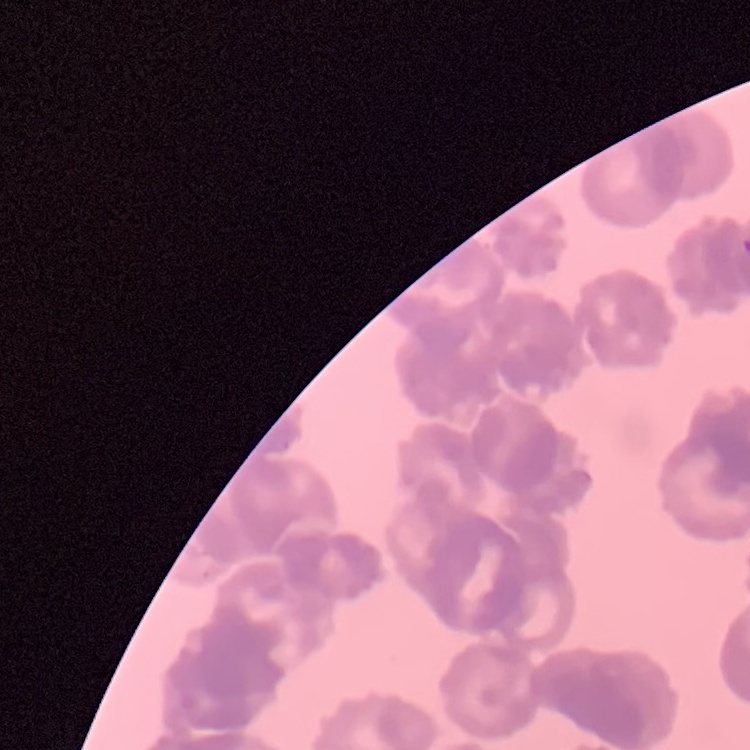
The red blood cells show rouleaux formation. Thin blood smear. Stained with either Field's or Giemsa. One tile cut from a larger photomicrograph.